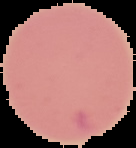
Summary:
  - Image type: segmented cell region with the area outside set to black
  - Preparation: thin blood film
  - Malaria status: uninfected
  - Image size: 136×148 pixels